Identify the parasite.
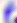

This is Toxoplasma gondii.

Micrograph. 400x magnification.